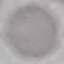
{
  "malaria_status": "uninfected",
  "image_type": "cell patch, automatically extracted from a larger field of view and resized to 64 × 64 pixels",
  "capture": "smartphone through the microscope eyepiece",
  "preparation": "thin smear",
  "stain": "Giemsa"
}